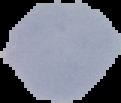
Cell region segmented out of the field of view; the surrounding area is masked to black. Image is 121×103 pixels. From a thin blood film. Malaria status: parasitized.